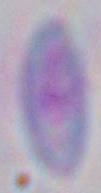
Summary:
  - Magnification: 1000x
  - Modality: micrograph
  - Identification: Toxoplasma gondii